Classify this cell by malaria status.
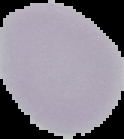
Uninfected.

Image is 124×139 pixels. From a thin blood smear. Segmented cell region on a black background.